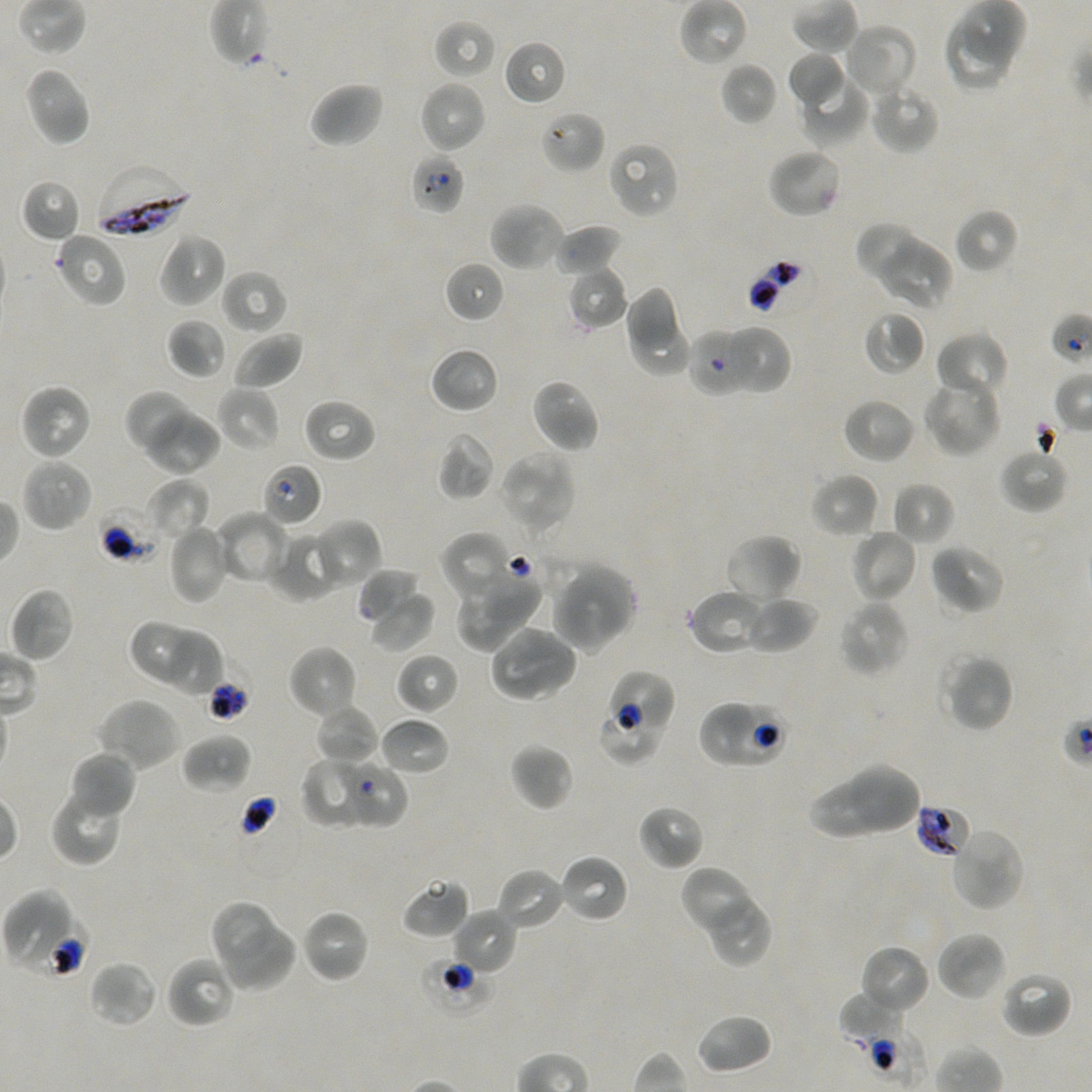
Approximate bounding rectangles given as corner coordinates in pixels from the top-left. Not every red blood cell is marked.
Summary:
  - Locations of red blood cells of indeterminate infection status: (x1=409, y1=152, x2=465, y2=215), (x1=1050, y1=312, x2=1092, y2=368), (x1=688, y1=327, x2=748, y2=397), (x1=262, y1=462, x2=323, y2=526), (x1=96, y1=506, x2=162, y2=564), (x1=190, y1=653, x2=249, y2=723), (x1=611, y1=668, x2=676, y2=738), (x1=700, y1=703, x2=758, y2=763), (x1=726, y1=704, x2=789, y2=766), (x1=339, y1=760, x2=407, y2=827), (x1=915, y1=803, x2=970, y2=858), (x1=3, y1=886, x2=69, y2=967), (x1=22, y1=917, x2=86, y2=976), (x1=421, y1=957, x2=494, y2=1013), (x1=839, y1=1024, x2=926, y2=1090)
  - Locations of infected red blood cells: (x1=92, y1=163, x2=192, y2=240)
  - Locations of uninfected red blood cells: (x1=434, y1=18, x2=497, y2=79), (x1=945, y1=20, x2=1009, y2=91), (x1=843, y1=22, x2=920, y2=100), (x1=503, y1=39, x2=567, y2=106), (x1=786, y1=51, x2=846, y2=108), (x1=721, y1=61, x2=777, y2=126), (x1=22, y1=65, x2=92, y2=148), (x1=795, y1=71, x2=869, y2=147), (x1=418, y1=79, x2=487, y2=153), (x1=307, y1=81, x2=384, y2=149), (x1=869, y1=82, x2=941, y2=153), (x1=541, y1=110, x2=605, y2=175), (x1=608, y1=141, x2=679, y2=219), (x1=766, y1=147, x2=843, y2=219), (x1=21, y1=179, x2=82, y2=243), (x1=488, y1=201, x2=566, y2=273), (x1=953, y1=207, x2=1018, y2=274), (x1=554, y1=223, x2=622, y2=277), (x1=859, y1=225, x2=920, y2=282), (x1=53, y1=231, x2=128, y2=308), (x1=157, y1=232, x2=228, y2=309), (x1=880, y1=240, x2=953, y2=311), (x1=443, y1=261, x2=505, y2=323), (x1=566, y1=266, x2=627, y2=330), (x1=220, y1=269, x2=288, y2=335), (x1=624, y1=285, x2=679, y2=352), (x1=863, y1=310, x2=925, y2=375), (x1=630, y1=316, x2=692, y2=377), (x1=166, y1=318, x2=226, y2=379), (x1=723, y1=326, x2=791, y2=395), (x1=232, y1=330, x2=304, y2=390), (x1=935, y1=331, x2=1010, y2=403), (x1=429, y1=347, x2=499, y2=414), (x1=530, y1=378, x2=600, y2=454), (x1=920, y1=378, x2=1002, y2=458), (x1=19, y1=382, x2=94, y2=460), (x1=216, y1=386, x2=281, y2=452), (x1=124, y1=390, x2=198, y2=456), (x1=302, y1=397, x2=376, y2=462), (x1=841, y1=397, x2=917, y2=465), (x1=143, y1=407, x2=221, y2=475), (x1=437, y1=431, x2=496, y2=500), (x1=998, y1=447, x2=1070, y2=513), (x1=500, y1=450, x2=577, y2=536), (x1=20, y1=457, x2=93, y2=532), (x1=809, y1=472, x2=881, y2=539), (x1=148, y1=478, x2=210, y2=543), (x1=892, y1=481, x2=956, y2=547), (x1=213, y1=510, x2=289, y2=585), (x1=313, y1=519, x2=382, y2=589), (x1=167, y1=524, x2=232, y2=604), (x1=850, y1=528, x2=918, y2=603), (x1=268, y1=530, x2=340, y2=602), (x1=439, y1=532, x2=515, y2=604), (x1=723, y1=532, x2=802, y2=605), (x1=928, y1=543, x2=1005, y2=616), (x1=566, y1=566, x2=637, y2=642), (x1=359, y1=567, x2=422, y2=623), (x1=484, y1=568, x2=542, y2=627), (x1=455, y1=575, x2=511, y2=651), (x1=551, y1=581, x2=627, y2=653), (x1=10, y1=587, x2=75, y2=663), (x1=688, y1=589, x2=767, y2=655), (x1=744, y1=594, x2=818, y2=655), (x1=369, y1=596, x2=435, y2=653), (x1=838, y1=600, x2=909, y2=678), (x1=129, y1=620, x2=198, y2=687), (x1=510, y1=624, x2=579, y2=691), (x1=166, y1=633, x2=225, y2=699), (x1=490, y1=640, x2=564, y2=702), (x1=288, y1=644, x2=359, y2=720), (x1=939, y1=651, x2=1015, y2=733), (x1=395, y1=652, x2=460, y2=715), (x1=97, y1=697, x2=183, y2=772), (x1=313, y1=703, x2=379, y2=767), (x1=600, y1=715, x2=660, y2=763), (x1=379, y1=716, x2=450, y2=776), (x1=181, y1=733, x2=252, y2=793), (x1=509, y1=742, x2=574, y2=811), (x1=67, y1=750, x2=136, y2=820), (x1=300, y1=757, x2=362, y2=828), (x1=850, y1=761, x2=921, y2=831), (x1=810, y1=778, x2=890, y2=839), (x1=49, y1=784, x2=126, y2=867), (x1=637, y1=804, x2=705, y2=871), (x1=949, y1=826, x2=1025, y2=912), (x1=558, y1=852, x2=630, y2=924), (x1=496, y1=867, x2=567, y2=932), (x1=679, y1=867, x2=750, y2=932), (x1=401, y1=877, x2=470, y2=940), (x1=714, y1=898, x2=770, y2=967), (x1=210, y1=900, x2=274, y2=964), (x1=300, y1=908, x2=371, y2=983), (x1=450, y1=908, x2=517, y2=976), (x1=225, y1=924, x2=295, y2=991), (x1=935, y1=930, x2=1007, y2=1002), (x1=858, y1=943, x2=930, y2=1017), (x1=165, y1=956, x2=236, y2=1029), (x1=89, y1=960, x2=159, y2=1027), (x1=1000, y1=971, x2=1073, y2=1038), (x1=839, y1=990, x2=907, y2=1043), (x1=695, y1=1013, x2=773, y2=1075)
  - Field of view: one from this slide
  - Culture: Plasmodium falciparum strain NF54, static, in vitro
  - Objective: 100x, oil immersion, numerical aperture 1.45
  - Donor blood group: A+/O+
  - Preparation: thin blood film
  - Image size: 1092×1092 pixels
  - Stain: Giemsa